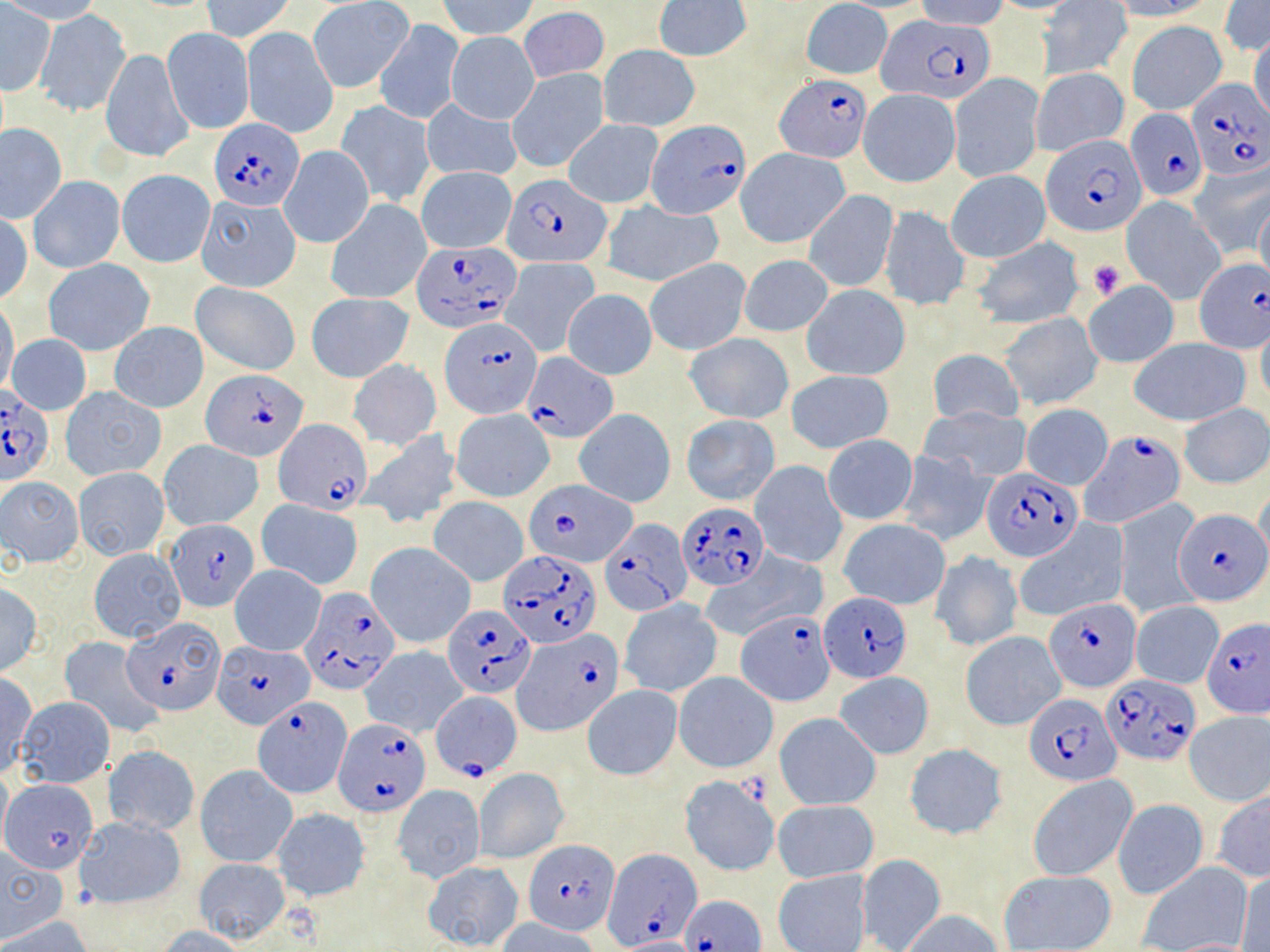

{
  "slide_level_diagnosis": "Plasmodium falciparum",
  "modality": "light microscopy",
  "image_size": "1270×952 pixels",
  "stain": "May-Grünwald-Giemsa",
  "uninfected_red_blood_cell_locations": "approximate bounding boxes as [x1, y1, x2, y2] in pixels: [0, 0, 106, 24], [200, 0, 296, 41], [439, 0, 539, 41], [800, 0, 893, 79], [989, 0, 1085, 14], [1112, 0, 1216, 20], [653, 1, 751, 62], [915, 1, 1009, 30], [1038, 1, 1131, 80], [310, 2, 410, 92], [1217, 2, 1270, 57], [1, 4, 55, 95], [518, 7, 610, 82], [37, 9, 131, 115], [375, 18, 463, 124], [1127, 20, 1226, 115], [242, 27, 338, 139], [162, 28, 254, 134], [446, 32, 539, 123], [1248, 32, 1270, 125], [599, 44, 700, 132], [101, 47, 193, 163], [508, 67, 611, 173], [1031, 68, 1129, 157], [949, 73, 1044, 182], [858, 89, 961, 188], [420, 99, 522, 183], [336, 101, 435, 208], [563, 119, 663, 207], [1, 123, 66, 222], [280, 145, 374, 248], [736, 147, 850, 249], [1187, 161, 1269, 257], [416, 166, 517, 253], [117, 169, 214, 268], [947, 169, 1050, 263], [28, 175, 124, 272], [802, 190, 899, 292], [195, 195, 300, 293], [325, 198, 431, 305], [1120, 198, 1226, 302], [1254, 198, 1270, 290], [603, 202, 722, 288], [879, 206, 968, 308], [1, 213, 33, 306], [972, 237, 1085, 329], [738, 254, 834, 337], [501, 257, 600, 357], [644, 258, 751, 357], [44, 259, 154, 356], [190, 281, 300, 375], [1083, 281, 1178, 367], [802, 286, 909, 382], [562, 289, 657, 380], [306, 293, 414, 382], [0, 300, 19, 396], [999, 312, 1103, 410], [1256, 319, 1270, 408], [109, 323, 208, 413], [6, 334, 91, 414], [684, 334, 794, 424], [1130, 337, 1251, 425], [928, 347, 1023, 426], [348, 358, 441, 450], [786, 370, 894, 453], [61, 386, 166, 481], [1178, 403, 1270, 488], [1021, 404, 1113, 489], [919, 405, 1032, 482], [574, 408, 675, 508], [450, 409, 555, 502], [681, 414, 780, 505], [357, 431, 462, 528], [823, 435, 918, 524], [158, 440, 263, 531], [894, 451, 996, 547], [750, 460, 847, 568], [73, 467, 171, 562], [0, 476, 85, 568], [1254, 487, 1270, 574], [257, 499, 364, 589], [429, 499, 528, 586], [1113, 500, 1202, 619], [839, 518, 950, 609], [1014, 521, 1130, 621], [367, 543, 475, 648], [88, 548, 185, 642], [930, 550, 1022, 652], [699, 551, 826, 644], [229, 565, 326, 656], [0, 582, 43, 677], [619, 598, 722, 698], [1130, 602, 1223, 689], [960, 631, 1066, 731], [60, 638, 162, 737], [361, 646, 469, 737], [674, 671, 778, 772], [0, 672, 37, 777], [835, 673, 934, 758], [582, 686, 682, 779], [13, 697, 114, 788], [1183, 712, 1270, 807], [776, 713, 881, 809], [902, 744, 1009, 839], [104, 745, 200, 838], [0, 763, 11, 851], [195, 764, 298, 868], [474, 768, 569, 863], [1027, 774, 1138, 882], [678, 776, 780, 877], [2, 779, 98, 872], [391, 785, 486, 883], [1211, 788, 1270, 882], [1112, 799, 1209, 900], [773, 800, 878, 882], [270, 808, 371, 902], [76, 815, 188, 909], [0, 852, 67, 940], [856, 854, 946, 952], [193, 858, 290, 943], [422, 860, 523, 951], [1137, 861, 1253, 952], [773, 868, 871, 952], [998, 870, 1116, 951], [1235, 870, 1270, 952], [902, 911, 1003, 952], [1, 916, 94, 951], [496, 917, 602, 952], [157, 926, 249, 952], [1164, 937, 1261, 951]",
  "magnification": "1000x",
  "platelet_locations": "approximate bounding boxes as [x1, y1, x2, y2] in pixels: [1088, 260, 1126, 300]",
  "field_of_view": "single",
  "preparation": "thin blood smear",
  "plasmodium_falciparum_infected_red_blood_cell_locations": "approximate bounding boxes as [x1, y1, x2, y2] in pixels: [877, 15, 998, 104], [776, 73, 870, 164], [1186, 80, 1270, 181], [1126, 108, 1208, 203], [209, 118, 306, 211], [647, 119, 749, 217], [1041, 133, 1147, 236], [505, 172, 609, 267], [411, 242, 522, 332], [1194, 259, 1268, 350], [441, 318, 542, 419], [523, 352, 620, 442], [203, 368, 307, 460], [0, 386, 54, 488], [273, 418, 374, 514], [1080, 431, 1187, 530], [982, 468, 1082, 561], [523, 481, 639, 568], [678, 503, 770, 590], [1176, 510, 1267, 606], [164, 518, 260, 613], [599, 519, 690, 617], [500, 550, 598, 647], [298, 585, 401, 695], [820, 592, 912, 683], [1044, 596, 1141, 692], [444, 606, 534, 698], [737, 609, 835, 704], [122, 617, 227, 714], [1200, 618, 1270, 719], [514, 629, 622, 734], [212, 640, 314, 728], [1102, 676, 1200, 765], [431, 690, 521, 779], [1023, 693, 1117, 787], [257, 696, 354, 800], [332, 719, 432, 816], [524, 840, 618, 931], [602, 845, 698, 952], [680, 895, 765, 952]"
}